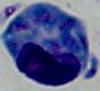

Photomicrograph. A white blood cell is seen. Captured at 1000x magnification.